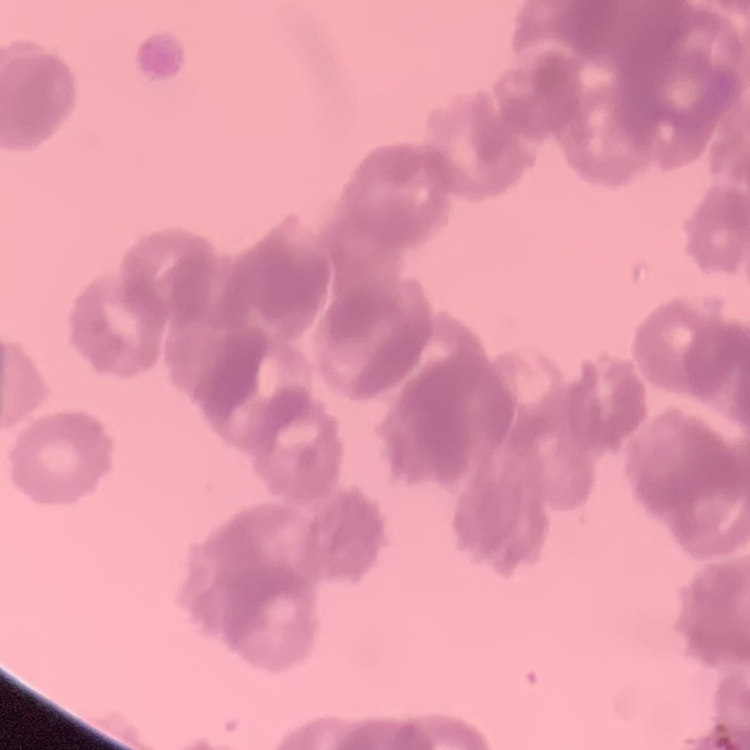
Summary:
  - Red blood cell morphology: rouleaux formation
  - Image type: one tile cut from a larger photomicrograph
  - Stain: Field's or Giemsa
  - Preparation: thin peripheral smear